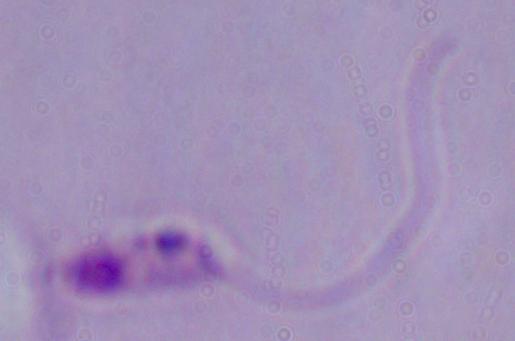
1000x magnification. A Leishmania parasite is shown. Photomicrograph.